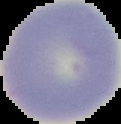
Summary:
  - Malaria status: uninfected
  - Preparation: thin blood smear
  - Image size: 121×124 pixels
  - Image type: segmented cell region with the area outside set to black